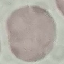

Malaria status: uninfected. Photographed with a smartphone camera at the microscope eyepiece. Thin blood smear. Automatically extracted cell patch, resized to 64 × 64 pixels. Giemsa-stained preparation.